Assess this cell for malaria.
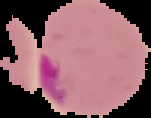
It is parasitized.

image_size: 151×118 pixels
preparation: thin blood film
image_type: cell region segmented out of the field of view; surrounding area masked to black